Identify the cell.
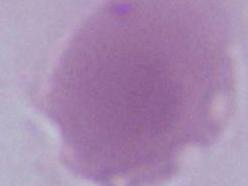
An erythrocyte.

modality = photomicrograph
magnification = 1000x